Report the malaria status of this cell.
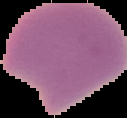
It is parasitized.

Summary:
  - Preparation: thin blood smear
  - Image type: cell region segmented out of the field of view; surrounding area masked to black
  - Image size: 127×118 pixels